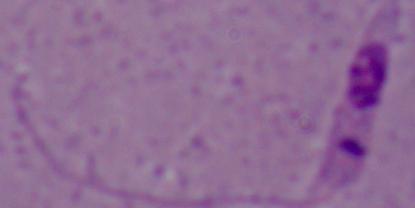
Summary:
  - Magnification: 1000x
  - Modality: photomicrograph
  - Identification: Leishmania